Locate every uninfected red blood cell.
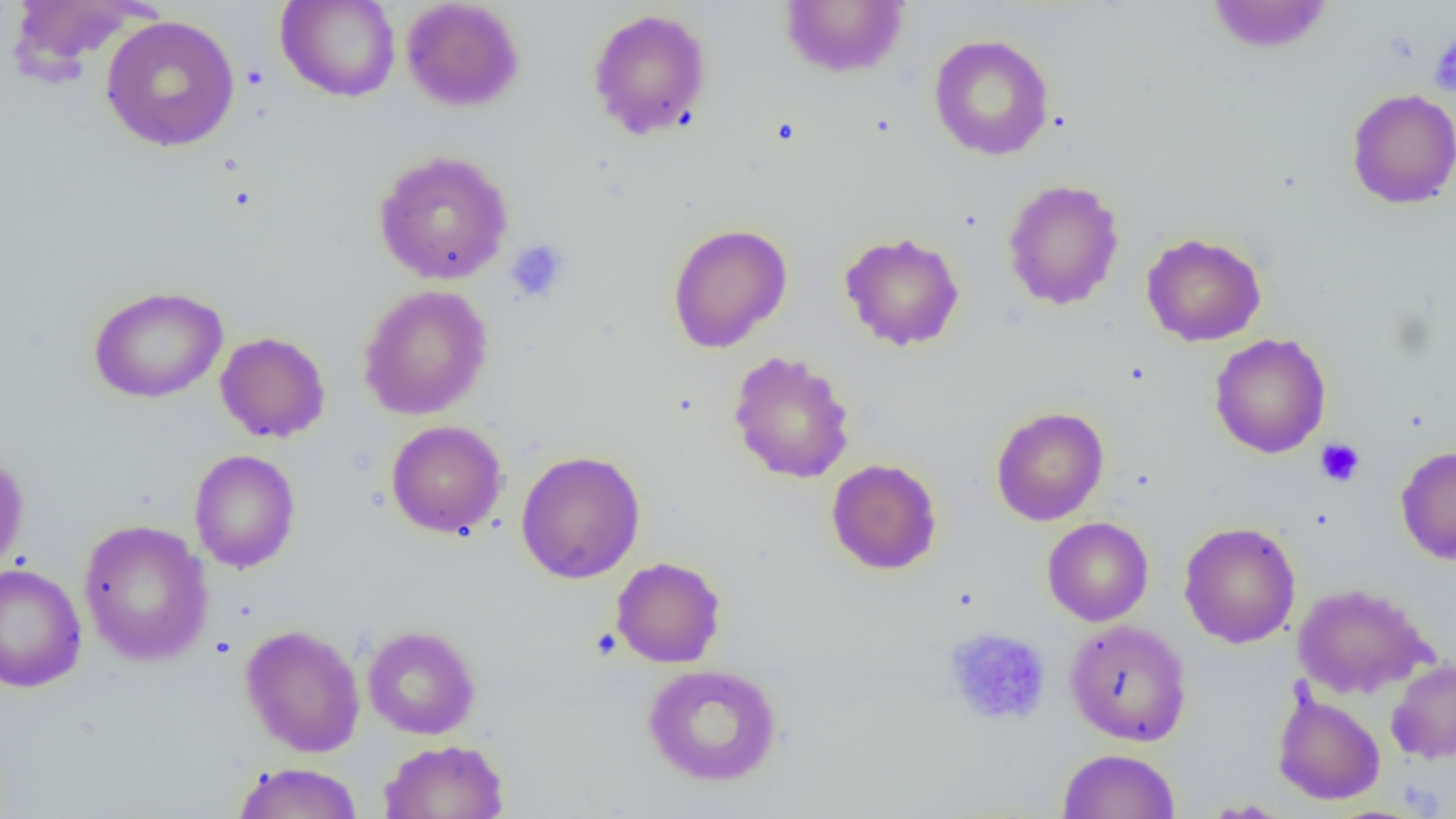
Approximate bounding boxes as (x1, y1, x2, y2) in pixels.
Uninfected red blood cells: (276, 0, 402, 102), (401, 0, 524, 111), (1206, 0, 1333, 53), (7, 1, 150, 80), (778, 1, 910, 78), (587, 8, 712, 141), (100, 15, 240, 153), (928, 34, 1054, 161), (1346, 88, 1456, 209), (373, 150, 513, 285), (1002, 178, 1125, 311), (667, 223, 793, 353), (839, 231, 965, 351), (1141, 232, 1267, 346), (88, 285, 227, 404), (358, 285, 493, 420), (215, 331, 330, 443), (1209, 333, 1331, 458), (728, 351, 855, 484), (991, 406, 1109, 526), (385, 420, 507, 538), (1395, 445, 1456, 565), (189, 449, 301, 573), (0, 450, 29, 574), (516, 450, 645, 583), (826, 459, 942, 575), (1042, 517, 1154, 626), (78, 519, 213, 666), (1178, 521, 1301, 649), (610, 556, 726, 668), (0, 562, 87, 693), (1293, 583, 1434, 699), (1066, 619, 1192, 746), (240, 624, 366, 757), (362, 625, 480, 739), (1386, 657, 1456, 764), (642, 663, 782, 786), (1273, 689, 1386, 805), (379, 739, 509, 819), (1057, 748, 1181, 819), (232, 762, 365, 819), (1197, 799, 1294, 817).

Summary:
  - Platelet locations: (1429, 35, 1456, 96), (505, 239, 570, 303), (1315, 438, 1365, 487), (942, 627, 1052, 727)
  - Slide-level diagnosis: negative for blood parasites
  - Preparation: thin blood film
  - Magnification: 1000x
  - Modality: optical microscopy
  - Field of view: one of a larger specimen
  - Image size: 1456×819 pixels